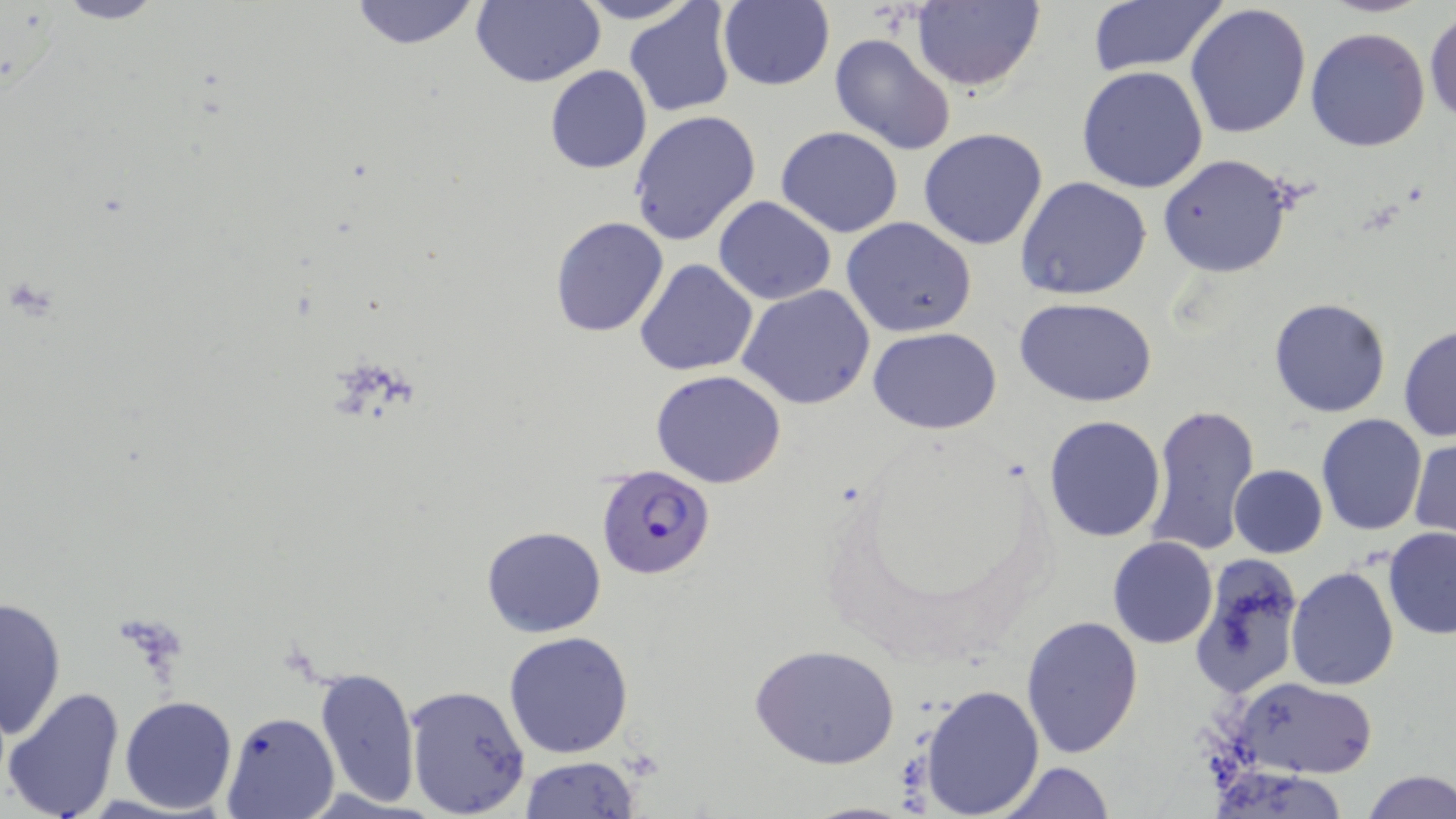
Summary:
  - Coordinate format: approximate bounding boxes as [x1, y1, x2, y2] in pixels
  - Plasmodium falciparum-infected red blood cell locations: [595, 463, 718, 581]
  - Uninfected red blood cell locations: [49, 0, 173, 25], [348, 0, 481, 51], [471, 0, 604, 87], [569, 0, 701, 25], [910, 0, 1043, 93], [717, 1, 835, 91], [623, 2, 739, 118], [1084, 2, 1227, 78], [1184, 3, 1312, 142], [1425, 11, 1456, 125], [1305, 26, 1432, 152], [829, 32, 957, 156], [544, 64, 652, 174], [1076, 66, 1209, 194], [629, 111, 762, 248], [776, 125, 904, 239], [917, 127, 1048, 251], [1156, 154, 1297, 278], [1015, 176, 1152, 301], [714, 198, 837, 305], [548, 216, 670, 338], [841, 217, 979, 339], [634, 259, 759, 376], [738, 284, 877, 410], [1014, 297, 1159, 405], [1269, 298, 1393, 418], [1398, 324, 1455, 442], [868, 326, 1003, 434], [649, 370, 788, 488], [1142, 403, 1259, 557], [1315, 412, 1427, 535], [1043, 414, 1165, 541], [1410, 437, 1455, 540], [1228, 464, 1328, 558], [480, 526, 606, 638], [1383, 528, 1456, 639], [1108, 537, 1217, 649], [1187, 554, 1304, 689], [1284, 565, 1399, 690], [1, 595, 67, 740], [1021, 616, 1145, 759], [504, 631, 635, 759], [750, 643, 901, 770], [314, 667, 420, 806], [1231, 676, 1378, 778], [920, 681, 1043, 816], [2, 684, 126, 819], [402, 684, 532, 817], [119, 695, 237, 814], [222, 712, 339, 818], [520, 756, 639, 818], [994, 761, 1116, 818], [1208, 763, 1355, 818], [1361, 769, 1456, 818], [799, 800, 919, 818]
  - Slide-level diagnosis: Plasmodium falciparum
  - Field of view: single
  - Modality: light microscopy
  - Image size: 1456×819 pixels
  - Stain: May-Grünwald-Giemsa
  - Magnification: 1000x
  - Preparation: thin blood smear